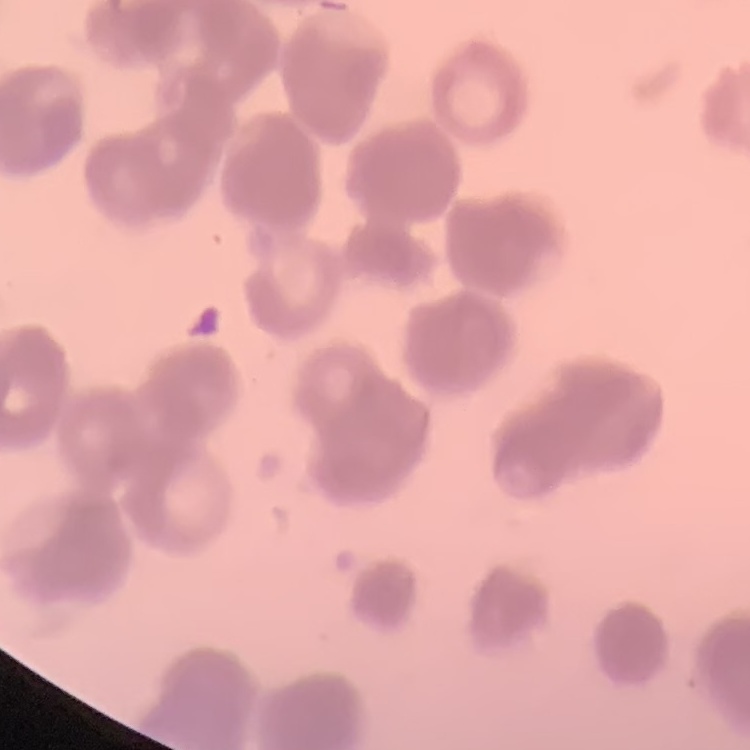

Summary:
  - Red blood cell morphology: rouleaux formation
  - Preparation: thin peripheral smear
  - Image type: one tile cut from a larger photomicrograph
  - Stain: Field's or Giemsa